Describe the morphology of the red blood cells.
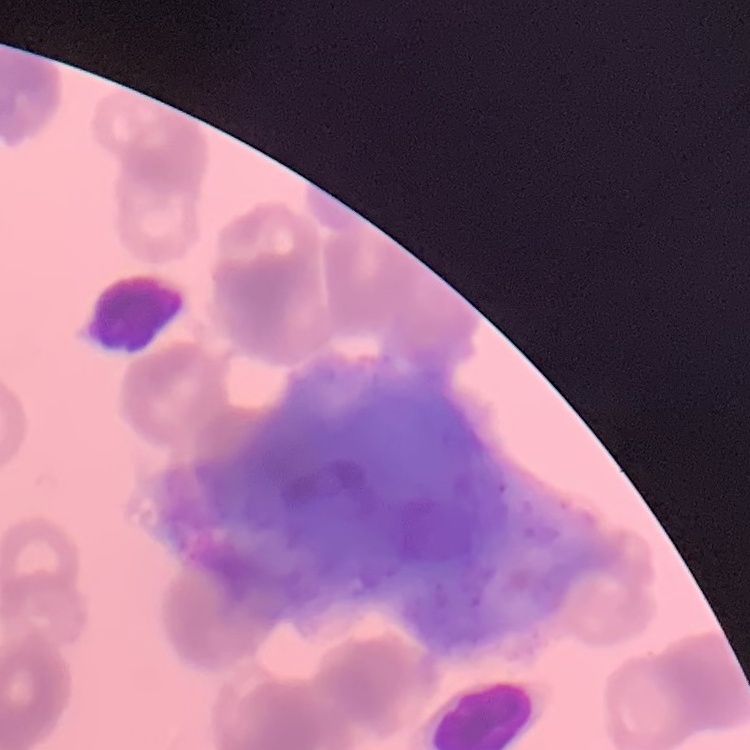

Rouleaux formation.

Summary:
  - Image type: one tile cut from a larger photomicrograph
  - Preparation: thin blood smear
  - Stain: Field's or Giemsa